Classify this cell by malaria status.
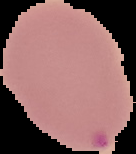

It is parasitized.

Image is 136×154 pixels. From a thin blood smear. Cell region segmented out of the field of view; the surrounding area is masked to black.